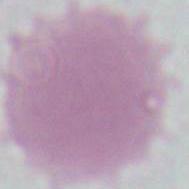

Summary:
  - Modality: photomicrograph
  - Magnification: 1000x
  - Identification: erythrocyte